Comment on the morphology of the red blood cells.
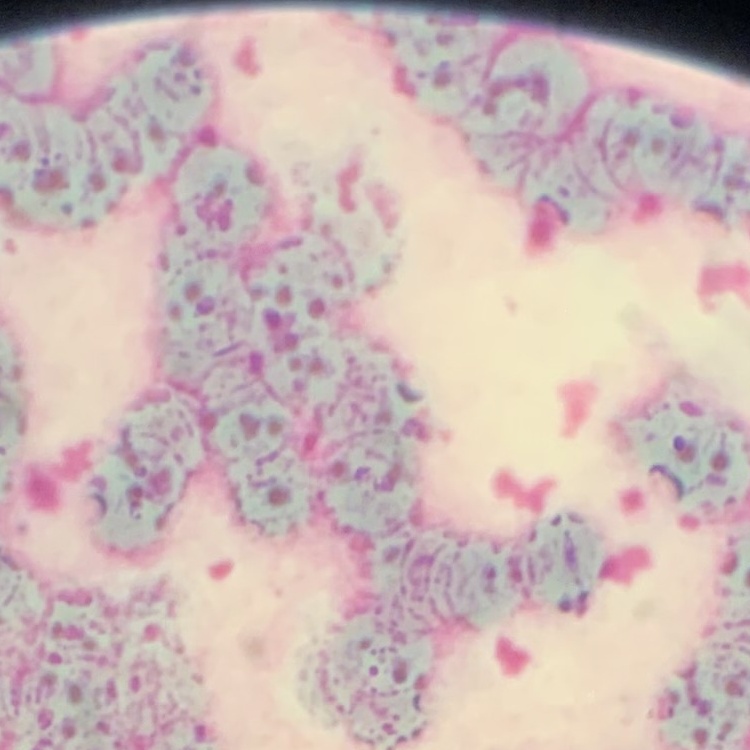

Rouleaux formation.

{
  "stain": "Field's or Giemsa",
  "image_type": "square crop of a larger photomicrograph",
  "preparation": "thin blood film"
}